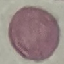
Result: negative for malaria parasites. Thin blood smear. Acquired by smartphone through the microscope eyepiece. Giemsa stain. Cell patch, automatically extracted from a larger field of view and resized to 64 × 64 pixels.